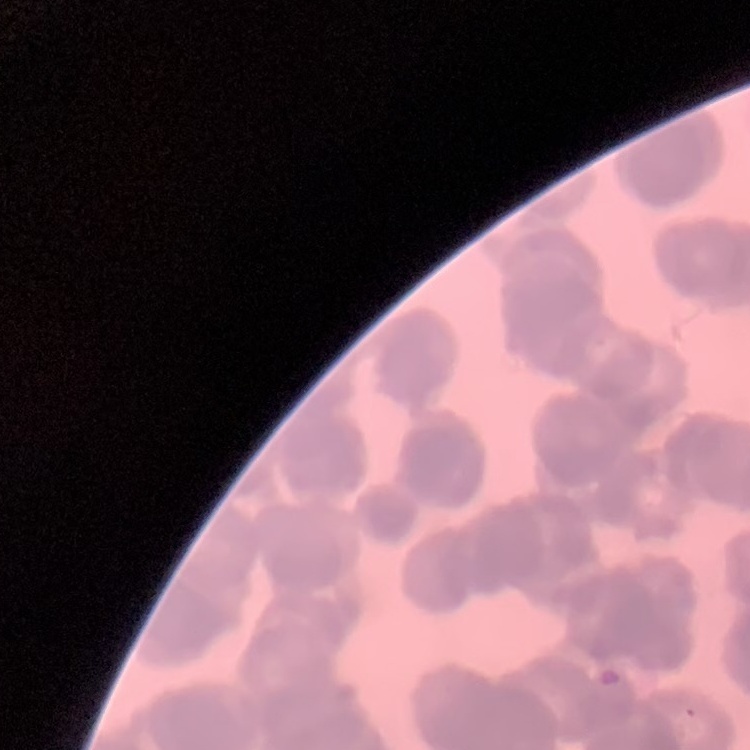

{
  "red_blood_cell_morphology": "rouleaux formation",
  "preparation": "thin blood film",
  "stain": "Field's or Giemsa",
  "image_type": "one tile cut from a larger photomicrograph"
}